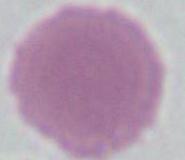

1000x magnification. A red blood cell is shown. Micrograph.